Report the malaria status of this cell.
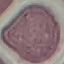
Uninfected.

image_type: cell patch, automatically extracted from a larger field of view and resized to 64 × 64 pixels
preparation: thin smear
capture: smartphone through the microscope eyepiece
stain: Giemsa